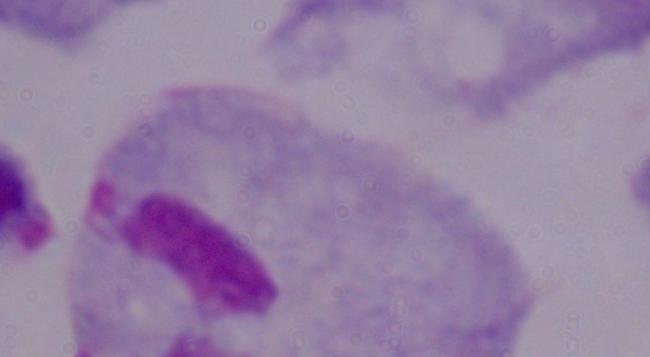

Summary:
  - Modality: micrograph
  - Identification: trichomonad
  - Magnification: 1000x